Describe the morphology of the red blood cells.
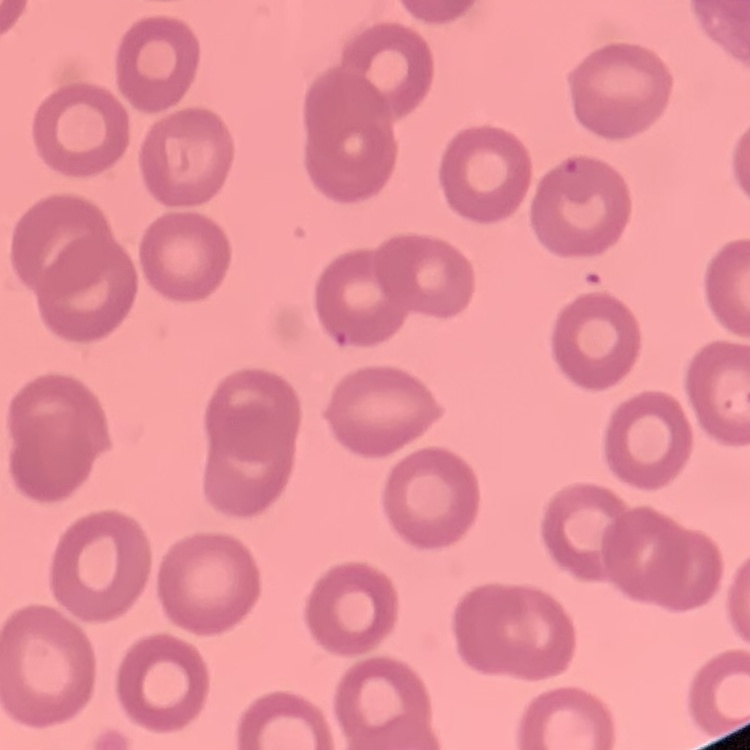
They show no rouleaux formation.

{
  "preparation": "thin blood film",
  "image_type": "square crop of a larger photomicrograph",
  "stain": "Field's or Giemsa"
}